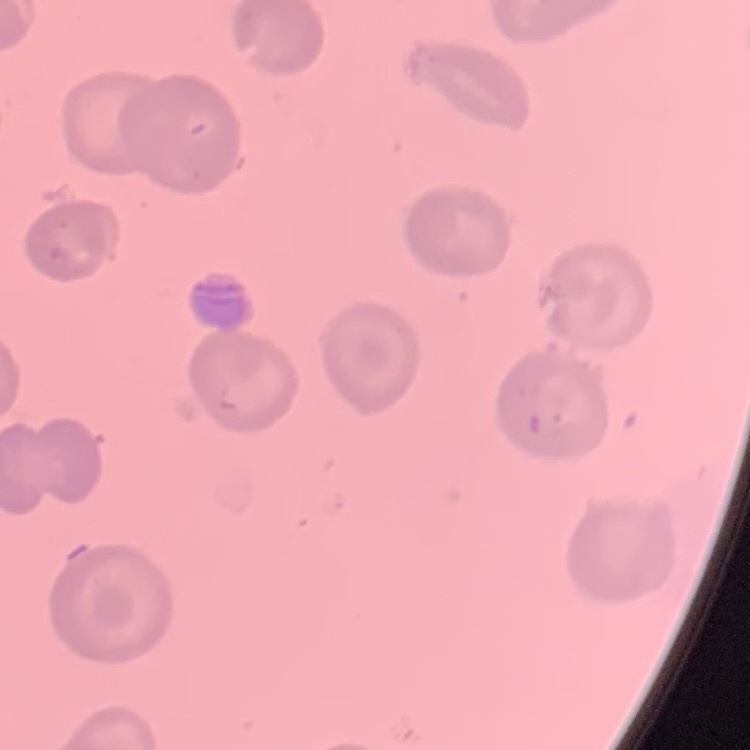

red blood cell morphology = no rouleaux formation
image type = square crop of a larger photomicrograph
stain = Field's or Giemsa
preparation = thin blood film